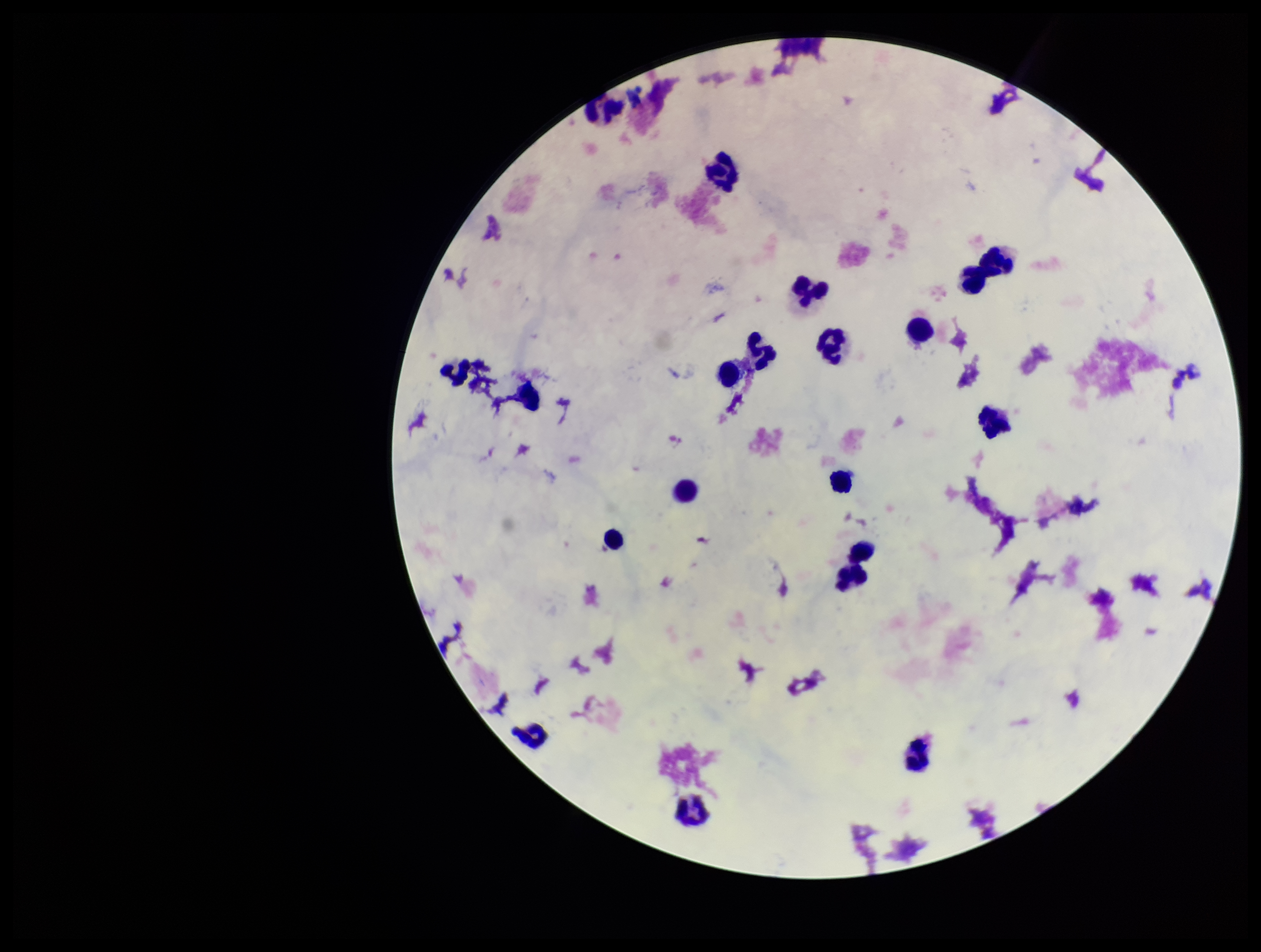
field_of_view: single
patient_malaria_status: negative
image_size: 1261×952 pixels
stain: Giemsa
leukocyte_count: 20
preparation: thick smear
capture: smartphone photograph through the microscope eyepiece
plasmodium_parasites: none identified
parasite_count: 0